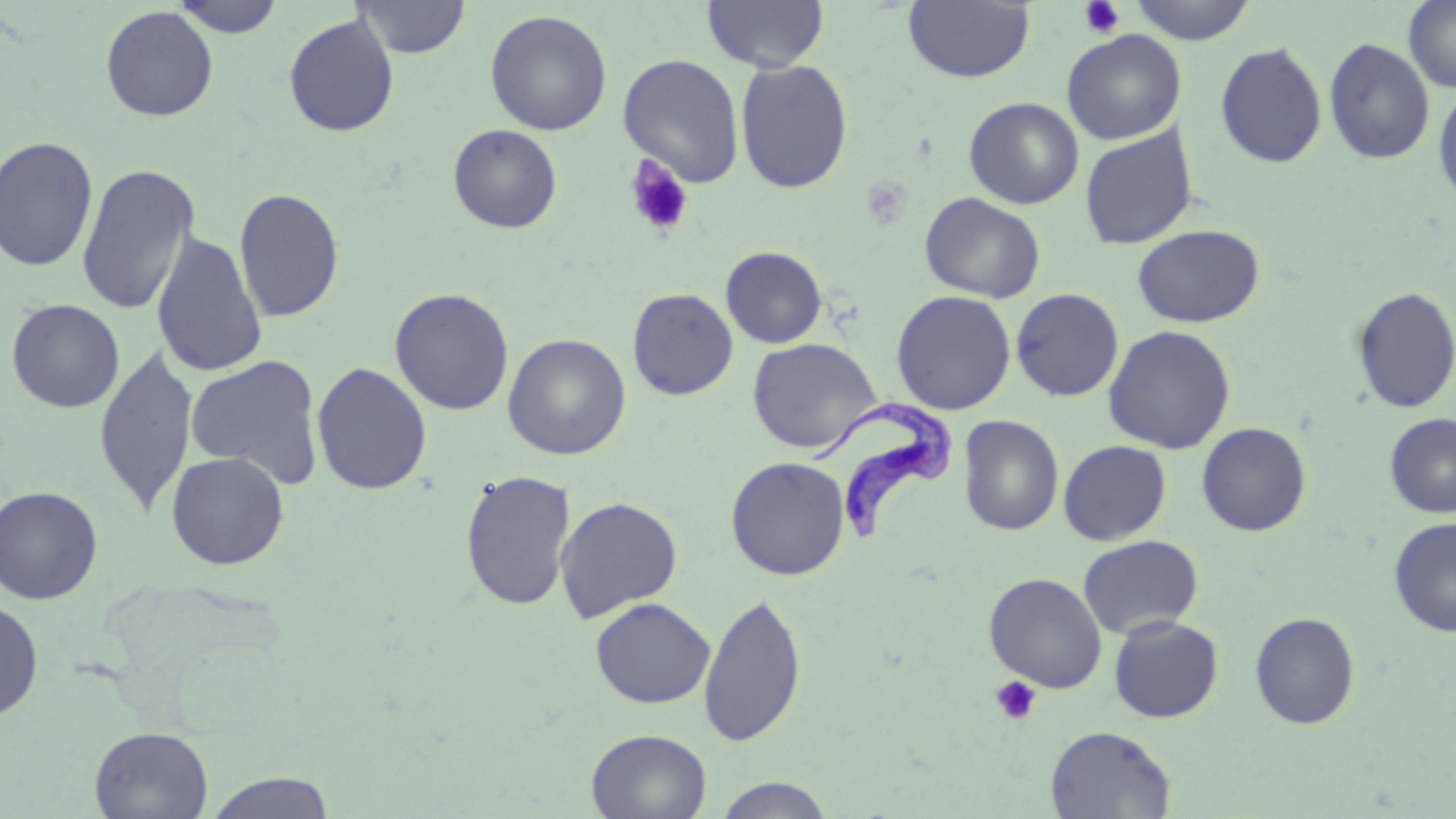

Summary:
  - Coordinate format: approximate bounding boxes as (x1,y1)-(x2,y2) corner pairs in pixels
  - Uninfected red blood cell locations: (170,0)-(285,38), (352,0)-(471,59), (702,0)-(829,72), (1126,0)-(1259,45), (1402,0)-(1456,93), (902,1)-(1035,84), (100,6)-(218,122), (484,9)-(613,136), (283,13)-(400,138), (1062,29)-(1186,145), (1323,37)-(1435,165), (1215,42)-(1328,168), (618,53)-(745,187), (735,59)-(853,194), (1433,83)-(1456,207), (963,97)-(1084,209), (448,124)-(563,233), (1079,125)-(1198,250), (0,136)-(98,273), (76,162)-(200,316), (233,187)-(345,323), (919,192)-(1046,303), (1132,225)-(1264,328), (150,230)-(268,379), (720,246)-(827,348), (1351,286)-(1456,414), (627,287)-(739,400), (389,288)-(514,415), (1010,288)-(1124,401), (890,290)-(1016,415), (6,298)-(125,413), (1103,325)-(1236,454), (502,333)-(631,460), (747,337)-(882,454), (93,345)-(199,518), (185,354)-(326,489), (311,361)-(432,495), (1384,413)-(1456,517), (958,415)-(1064,536), (1196,421)-(1312,537), (1058,440)-(1171,545), (166,451)-(289,570), (725,456)-(850,580), (460,469)-(577,612), (0,485)-(103,605), (554,496)-(683,622), (1388,517)-(1456,636), (1078,535)-(1204,639), (984,572)-(1107,693), (698,592)-(808,748), (590,597)-(715,708), (0,599)-(44,722), (1249,611)-(1361,729), (1108,615)-(1224,723), (1044,725)-(1177,818), (89,726)-(213,818), (586,728)-(712,818), (204,771)-(337,817), (711,775)-(836,818)
  - Trypanosoma brucei locations: (813,399)-(961,550)
  - Platelet locations: (1079,0)-(1125,39), (624,156)-(694,238), (990,675)-(1042,726)
  - Slide-level diagnosis: Trypanosoma brucei
  - Modality: optical microscopy
  - Preparation: thin blood film
  - Magnification: 1000x
  - Image size: 1456×819 pixels
  - Field of view: single
  - Stain: May-Grünwald-Giemsa